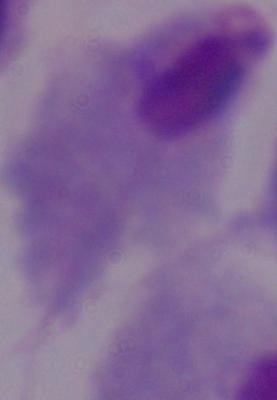
identification = trichomonad
modality = micrograph
magnification = 1000x